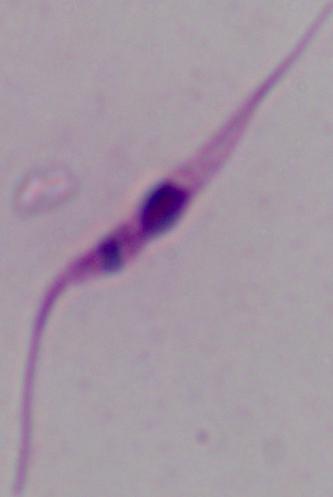

Photomicrograph. A Leishmania parasite is seen. Captured at 1000x magnification.